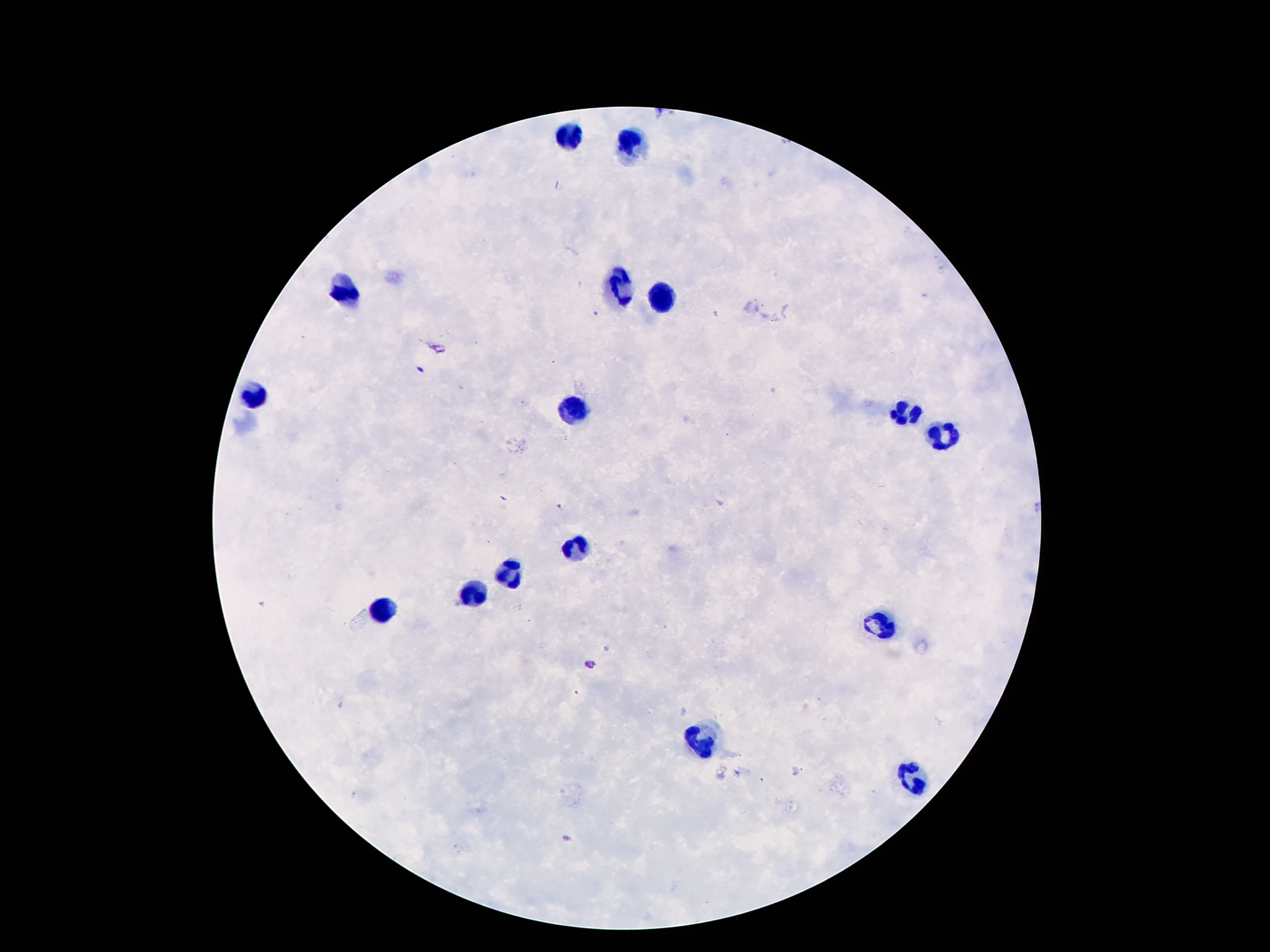

Approximate centers as (x, y) in pixels.
Summary:
  - Leukocyte locations: (569, 136), (632, 145), (618, 290), (345, 294), (664, 297), (249, 397), (573, 409), (904, 414), (944, 437), (573, 548), (510, 573), (477, 592), (382, 606), (886, 622), (699, 741), (909, 781)
  - Patient malaria status: not infected
  - Stain: Giemsa
  - Preparation: thick blood smear
  - Capture: smartphone camera through the microscope eyepiece
  - Image size: 1270×952 pixels
  - Field of view: one from this slide
  - Magnification: 100x